Identify the parasite.
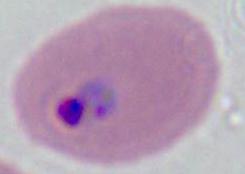

Plasmodium.

Summary:
  - Modality: photomicrograph
  - Magnification: 400x or 1000x